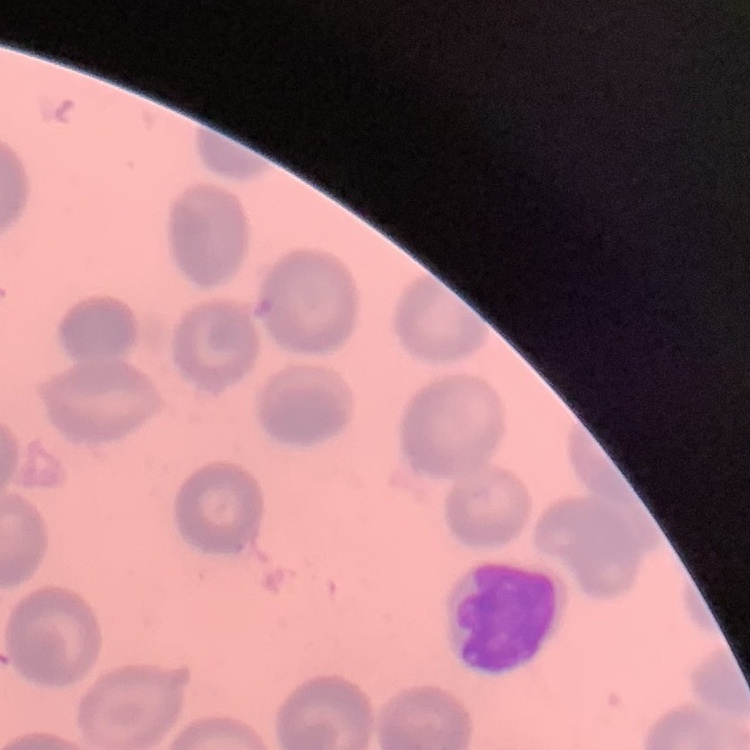
The red blood cells exhibit no rouleaux formation. Square crop of a larger photomicrograph. Thin peripheral smear. Field's or Giemsa stain.